Report the malaria status of this cell.
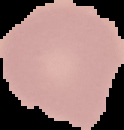
Uninfected.

Summary:
  - Image size: 124×130 pixels
  - Preparation: thin blood film
  - Image type: cell region segmented out of the field of view; surrounding area masked to black